Assess the morphology of the red blood cells.
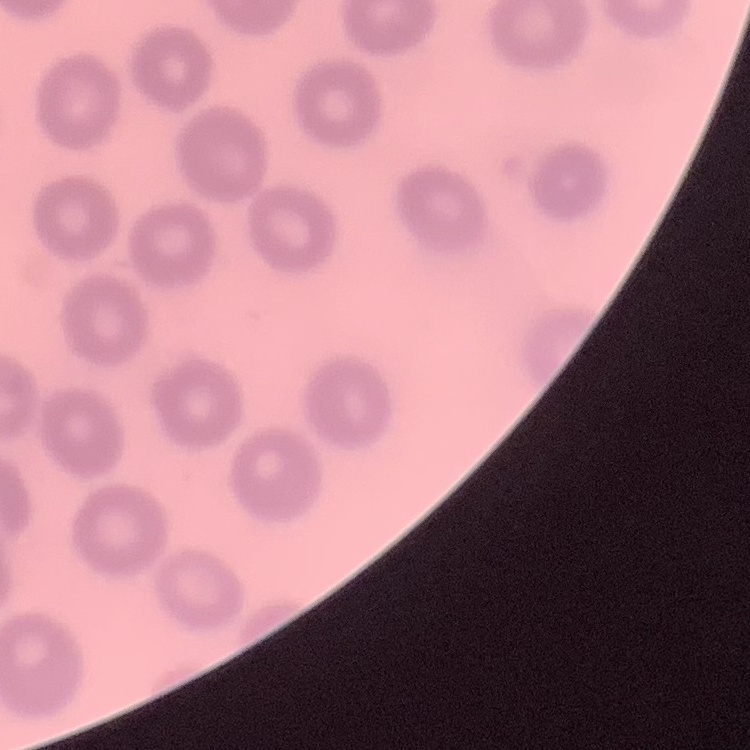

No rouleaux formation.

stain = Field's or Giemsa
image type = one tile cut from a larger photomicrograph
preparation = thin blood smear